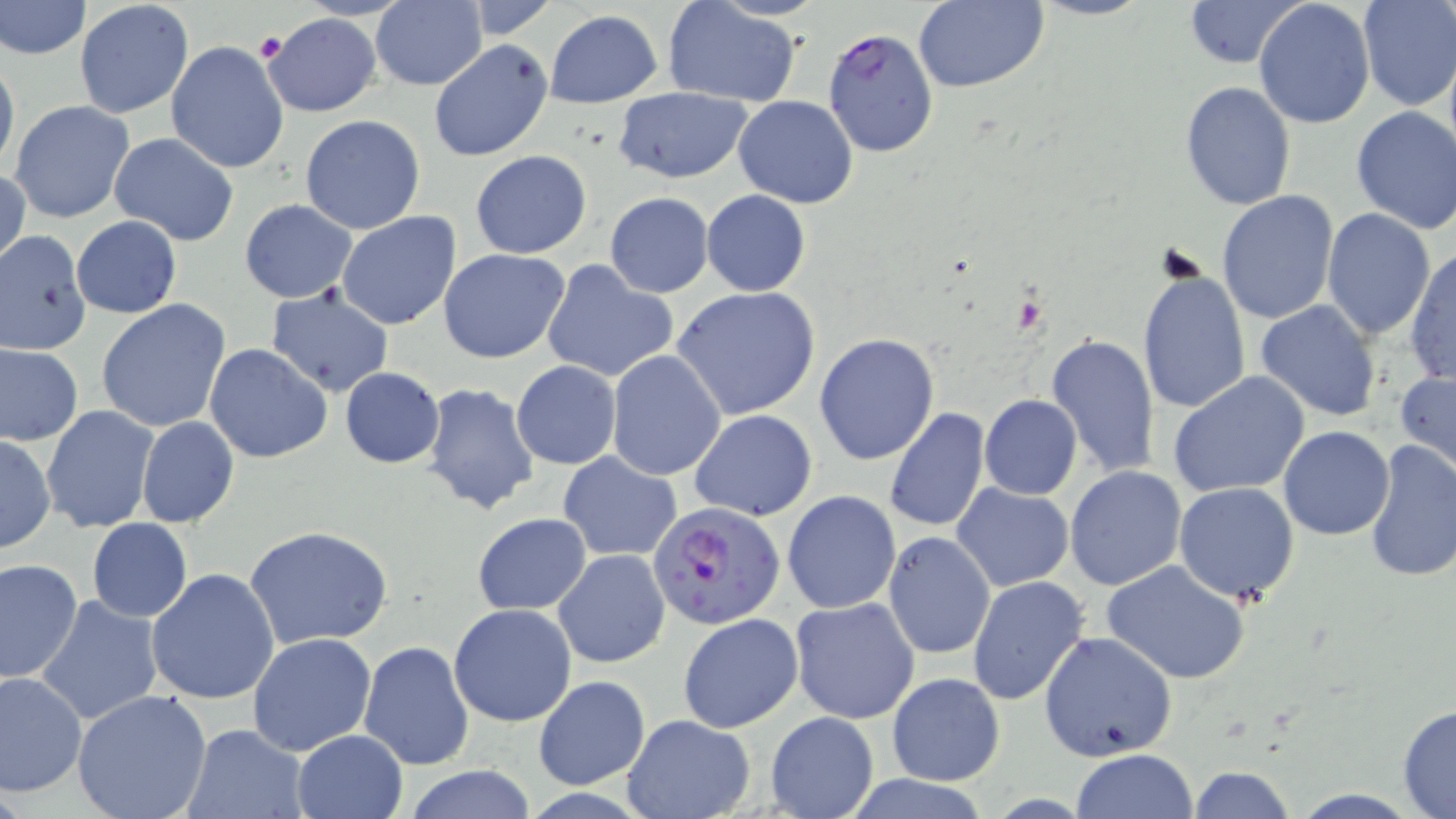 Approximate bounding boxes as [x1, y1, x2, y2] in pixels. Platelet locations: [255, 31, 288, 63]. Plasmodium falciparum-infected red blood cell locations: [822, 28, 939, 159], [648, 503, 786, 630]. Uninfected red blood cell locations: [0, 0, 90, 61], [74, 0, 193, 119], [460, 0, 559, 38], [1027, 0, 1153, 21], [1181, 0, 1309, 68], [1357, 0, 1455, 111], [369, 1, 486, 90], [661, 1, 804, 108], [912, 1, 1047, 93], [1253, 1, 1375, 129], [544, 9, 663, 109], [260, 13, 381, 117], [429, 39, 553, 162], [166, 40, 289, 173], [1443, 43, 1456, 168], [0, 52, 20, 178], [1180, 80, 1295, 212], [613, 88, 753, 181], [733, 96, 857, 206], [9, 100, 136, 224], [1350, 105, 1456, 234], [300, 114, 425, 235], [108, 132, 239, 245], [469, 151, 592, 259], [1, 165, 29, 274], [701, 190, 811, 296], [1217, 190, 1340, 325], [605, 192, 714, 298], [240, 200, 356, 303], [1321, 208, 1435, 340], [336, 212, 462, 331], [71, 216, 181, 318], [0, 231, 92, 354], [1407, 245, 1455, 385], [439, 247, 570, 363], [540, 261, 679, 385], [1137, 263, 1253, 417], [672, 286, 821, 421], [266, 287, 394, 398], [97, 299, 233, 434], [1254, 299, 1383, 421], [814, 334, 941, 466], [1043, 334, 1161, 477], [2, 343, 83, 446], [203, 344, 331, 464], [606, 350, 725, 480], [512, 361, 621, 469], [338, 367, 446, 468], [1396, 369, 1456, 481], [1168, 372, 1311, 499], [423, 383, 541, 516], [978, 394, 1082, 500], [41, 405, 160, 534], [884, 407, 991, 533], [690, 409, 818, 522], [137, 416, 239, 528], [1279, 426, 1395, 541], [1, 435, 55, 554], [1363, 438, 1456, 584], [559, 451, 681, 562], [1064, 466, 1186, 591], [1174, 482, 1301, 604], [952, 485, 1074, 592], [782, 490, 901, 614], [472, 511, 592, 614], [87, 519, 193, 622], [245, 525, 395, 650], [883, 532, 995, 659], [554, 549, 671, 667], [0, 558, 82, 685], [1102, 560, 1252, 684], [145, 568, 280, 705], [967, 576, 1091, 706], [37, 595, 163, 726], [789, 597, 920, 723], [449, 603, 577, 727], [678, 612, 802, 734], [1039, 631, 1178, 762], [249, 632, 378, 756], [359, 640, 475, 770], [0, 670, 86, 797], [886, 673, 1004, 786], [534, 674, 650, 790], [72, 689, 213, 819], [1397, 704, 1456, 817], [766, 711, 879, 819], [620, 713, 755, 819], [183, 723, 308, 818], [292, 730, 407, 817], [1070, 749, 1199, 819], [402, 765, 538, 819], [1186, 765, 1295, 819]. Slide-level diagnosis: Plasmodium falciparum. May-Grünwald-Giemsa stain. Single field of view. Thin blood smear. Image is 1456×819 pixels. Optical microscopy. Captured at 1000x magnification.